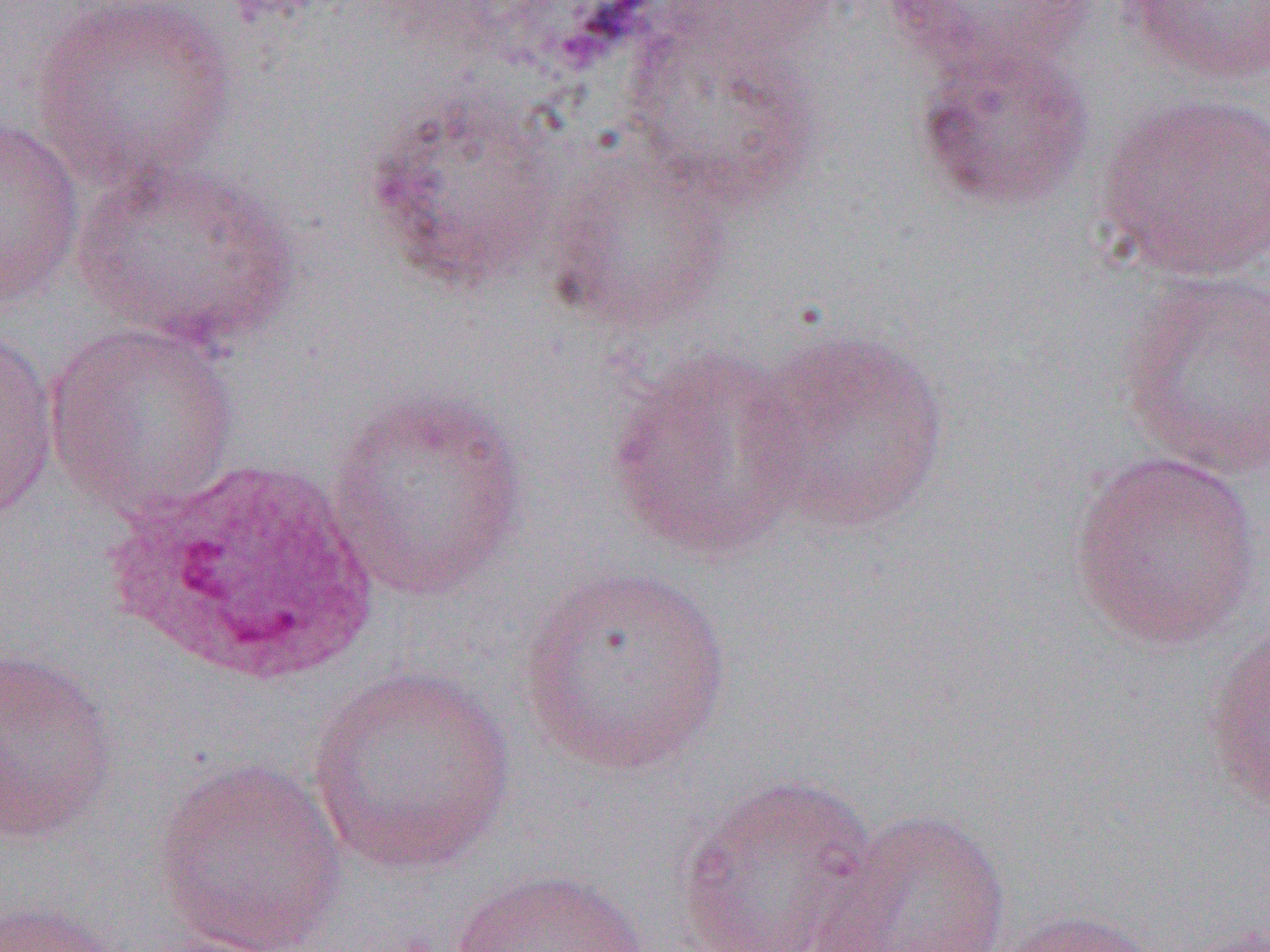
Summary:
  - Coordinate format: approximate bounding boxes as [x1, y1, x2, y2] in pixels
  - Uninfected red blood cell locations: [27, 0, 240, 191], [883, 0, 1099, 79], [1120, 1, 1270, 86], [620, 21, 823, 212], [911, 35, 1097, 216], [364, 89, 572, 292], [1095, 91, 1270, 281], [0, 118, 86, 311], [544, 149, 732, 331], [67, 153, 303, 352], [1117, 270, 1270, 482], [44, 320, 241, 521], [0, 326, 60, 525], [742, 326, 951, 536], [606, 352, 809, 562], [324, 388, 528, 601], [1068, 451, 1265, 650], [515, 564, 737, 778], [1202, 619, 1270, 817], [0, 643, 119, 847], [304, 665, 517, 875], [152, 757, 350, 952], [674, 773, 882, 951], [812, 808, 1012, 951], [449, 867, 650, 952], [0, 900, 120, 952], [987, 907, 1161, 952], [1166, 922, 1270, 952]
  - White blood cell locations: [98, 455, 386, 693]
  - Slide-level diagnosis: Plasmodium ovale
  - Image size: 1270×952 pixels
  - Field of view: single
  - Preparation: thin blood film
  - Modality: light microscopy
  - Magnification: 1000x